Assess this cell for malaria.
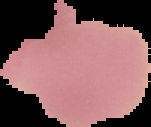
Uninfected.

Summary:
  - Image size: 151×127 pixels
  - Preparation: thin blood film
  - Image type: segmented cell region with the area outside set to black